Name the parasite shown.
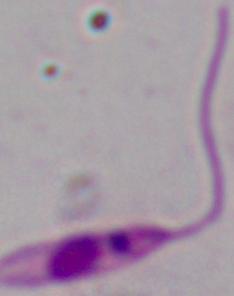

This is Leishmania.

Micrograph. 1000x magnification.